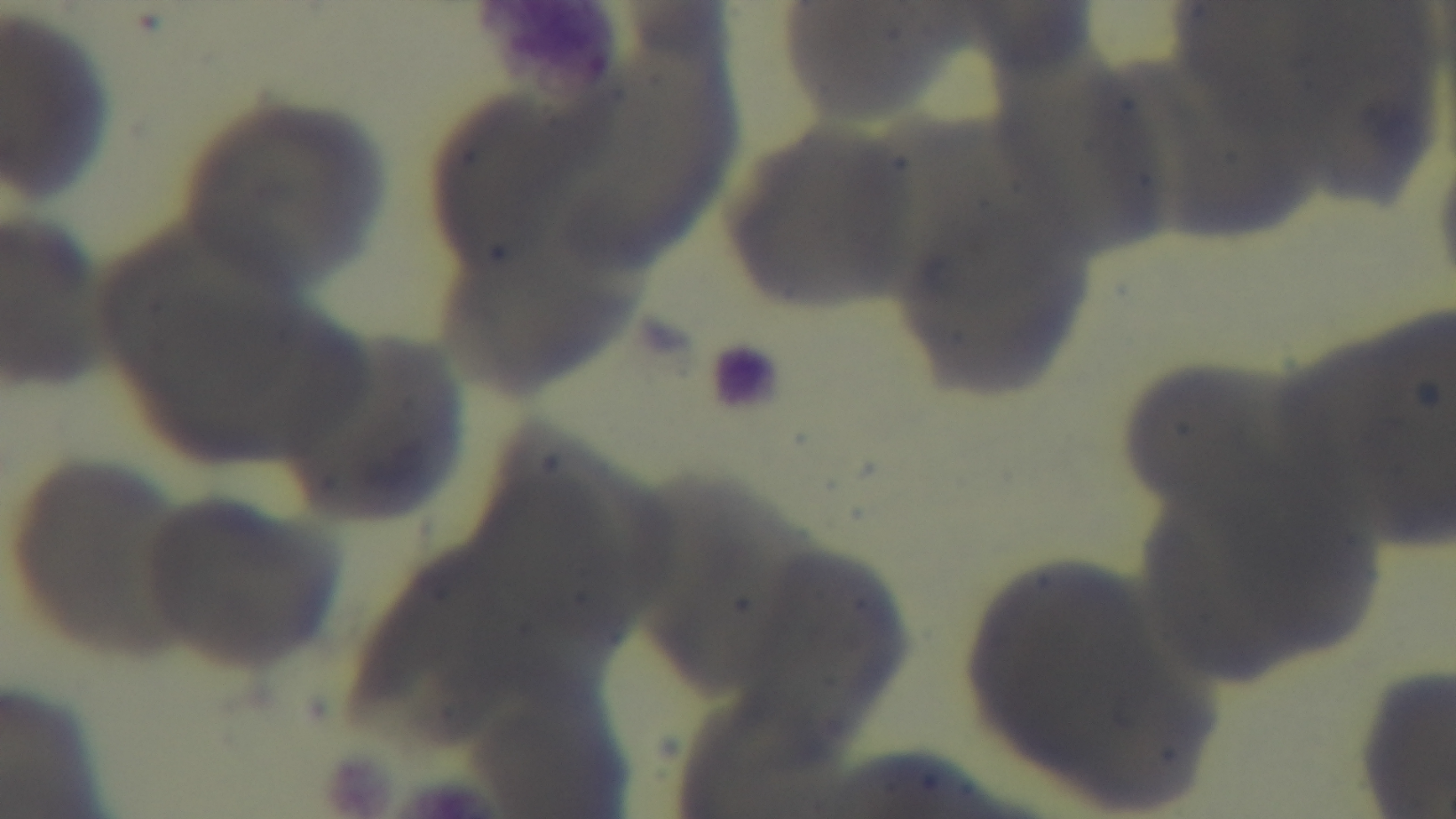
{
  "capture": "mounted 4K digital camera",
  "stain": "Giemsa",
  "modality": "light microscopy",
  "malaria_status": "negative",
  "field_of_view": "single",
  "objective": "100x oil immersion",
  "preparation": "thin blood film"
}